Assess this cell for malaria.
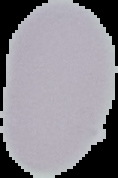
It is uninfected.

Summary:
  - Preparation: thin blood smear
  - Image type: cell region segmented out of the field of view; surrounding area masked to black
  - Image size: 118×178 pixels